Report the malaria status of this cell.
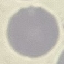
Uninfected.

Summary:
  - Image type: cell patch, automatically extracted from a larger field of view and resized to 64 × 64 pixels
  - Preparation: thin blood smear
  - Capture: smartphone through the microscope eyepiece
  - Stain: Giemsa